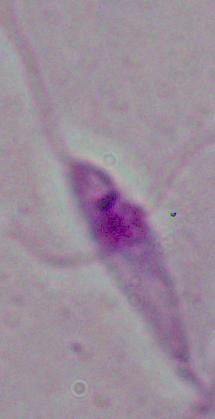

Summary:
  - Magnification: 1000x
  - Modality: micrograph
  - Identification: Leishmania